Assess this cell for malaria.
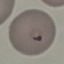
Parasitized.

Photographed with a smartphone camera at the microscope eyepiece. Giemsa stain. Automatically extracted cell patch, resized to 64 × 64 pixels. Thin blood smear.